Locate and identify every blood parasite.
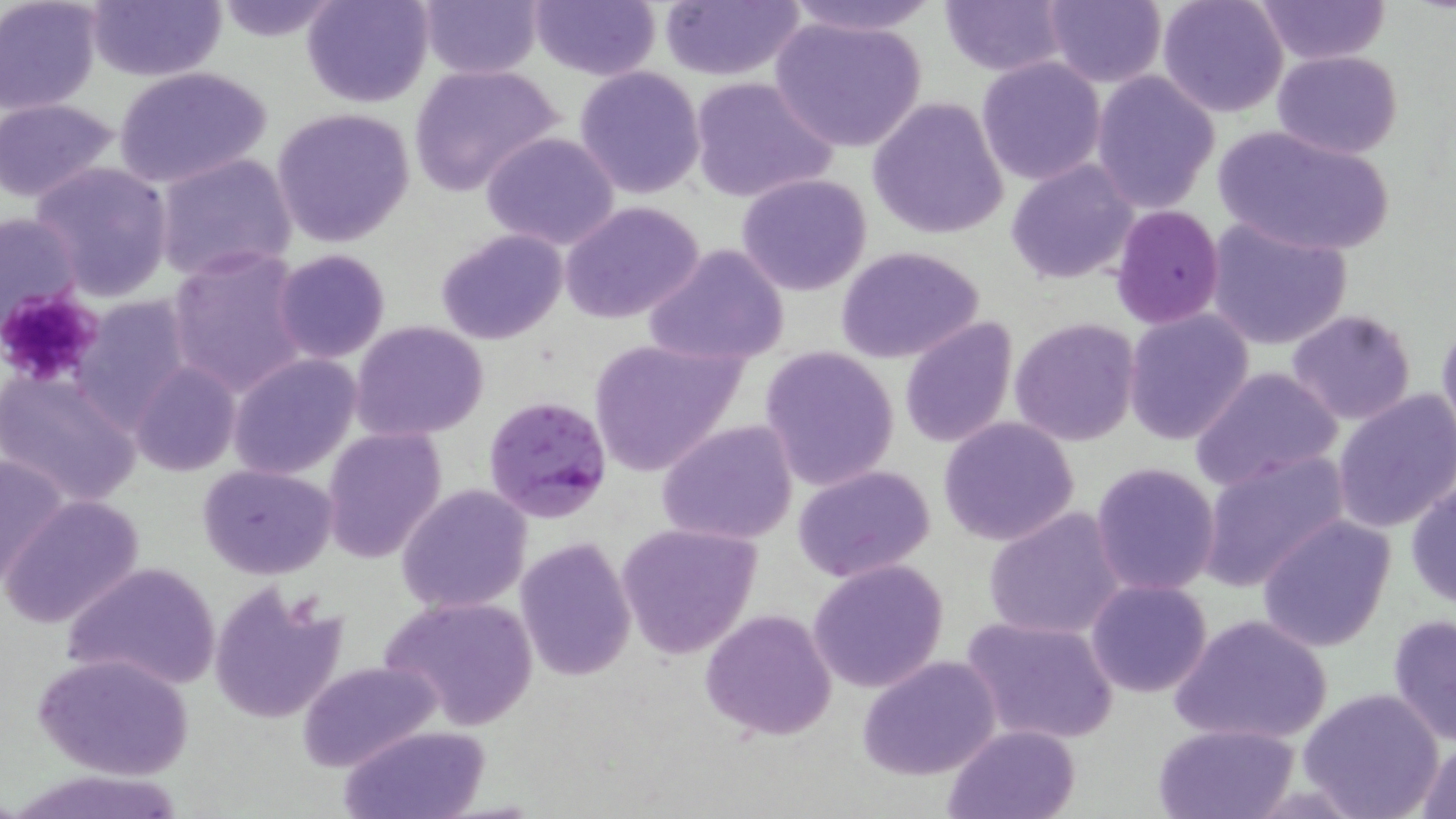
Approximate bounding boxes as (x1,y1)-(x2,y2) corner pairs in pixels.
Plasmodium falciparum-infected red blood cells: (484,393)-(616,524).
No Plasmodium ovale, Plasmodium malariae, Plasmodium vivax, Babesia divergens, or Trypanosoma brucei observed.

slide_level_diagnosis: Plasmodium falciparum
platelet_locations: 'approximate bounding boxes as (x1,y1)-(x2,y2) corner pairs in pixels: (0,288)-(107,387)'
preparation: thin blood smear
modality: light microscopy
image_size: 1456×819 pixels
magnification: 1000x
stain: May-Grünwald-Giemsa
field_of_view: single
uninfected_red_blood_cell_locations: 'approximate bounding boxes as (x1,y1)-(x2,y2) corner pairs in pixels: (1,0)-(101,114), (85,0)-(228,83), (302,0)-(435,108), (417,0)-(543,79), (659,0)-(804,80), (778,0)-(944,37), (937,0)-(1068,75), (1042,0)-(1165,89), (1157,0)-(1289,118), (209,1)-(346,44), (528,1)-(660,81), (1253,1)-(1389,65), (771,15)-(926,154), (1272,50)-(1403,159), (977,57)-(1106,185), (408,64)-(563,195), (574,65)-(707,200), (114,67)-(270,189), (1090,71)-(1220,213), (688,76)-(838,204), (867,95)-(1009,238), (0,99)-(119,203), (272,107)-(415,249), (1212,123)-(1395,258), (480,130)-(622,250), (154,151)-(300,284), (1006,158)-(1140,283), (30,162)-(175,300), (736,173)-(874,296), (559,201)-(706,325), (1109,206)-(1227,330), (1,212)-(83,326), (1204,217)-(1352,351), (435,229)-(569,346), (645,243)-(790,367), (835,245)-(987,365), (167,246)-(310,396), (271,249)-(392,363), (69,296)-(196,430), (1122,308)-(1255,446), (1284,308)-(1420,426), (1435,315)-(1456,446), (1009,316)-(1142,448), (897,317)-(1017,449), (350,321)-(490,440), (587,337)-(746,476), (759,346)-(901,491), (228,353)-(361,480), (131,361)-(240,478), (1190,367)-(1343,490), (2,371)-(143,505), (1332,390)-(1456,534), (937,416)-(1081,547), (655,418)-(799,546), (323,426)-(448,563), (0,451)-(70,585), (1198,451)-(1350,588), (1090,461)-(1220,596), (197,463)-(339,579), (792,465)-(938,583), (1407,479)-(1456,608), (396,483)-(532,613), (2,495)-(146,631), (984,508)-(1127,641), (1257,514)-(1395,652), (615,523)-(762,659), (514,537)-(635,681), (807,558)-(950,694), (59,561)-(221,693), (1085,578)-(1213,698), (209,579)-(350,724), (379,595)-(539,731), (700,607)-(838,740), (1170,613)-(1333,745), (1387,613)-(1456,745), (959,615)-(1120,745), (34,652)-(194,780), (858,656)-(1003,780), (296,658)-(443,774), (1298,686)-(1444,819), (1153,721)-(1301,817), (340,724)-(490,817), (942,724)-(1082,818), (1411,739)-(1456,818)'